Point out each Plasmodium parasite.
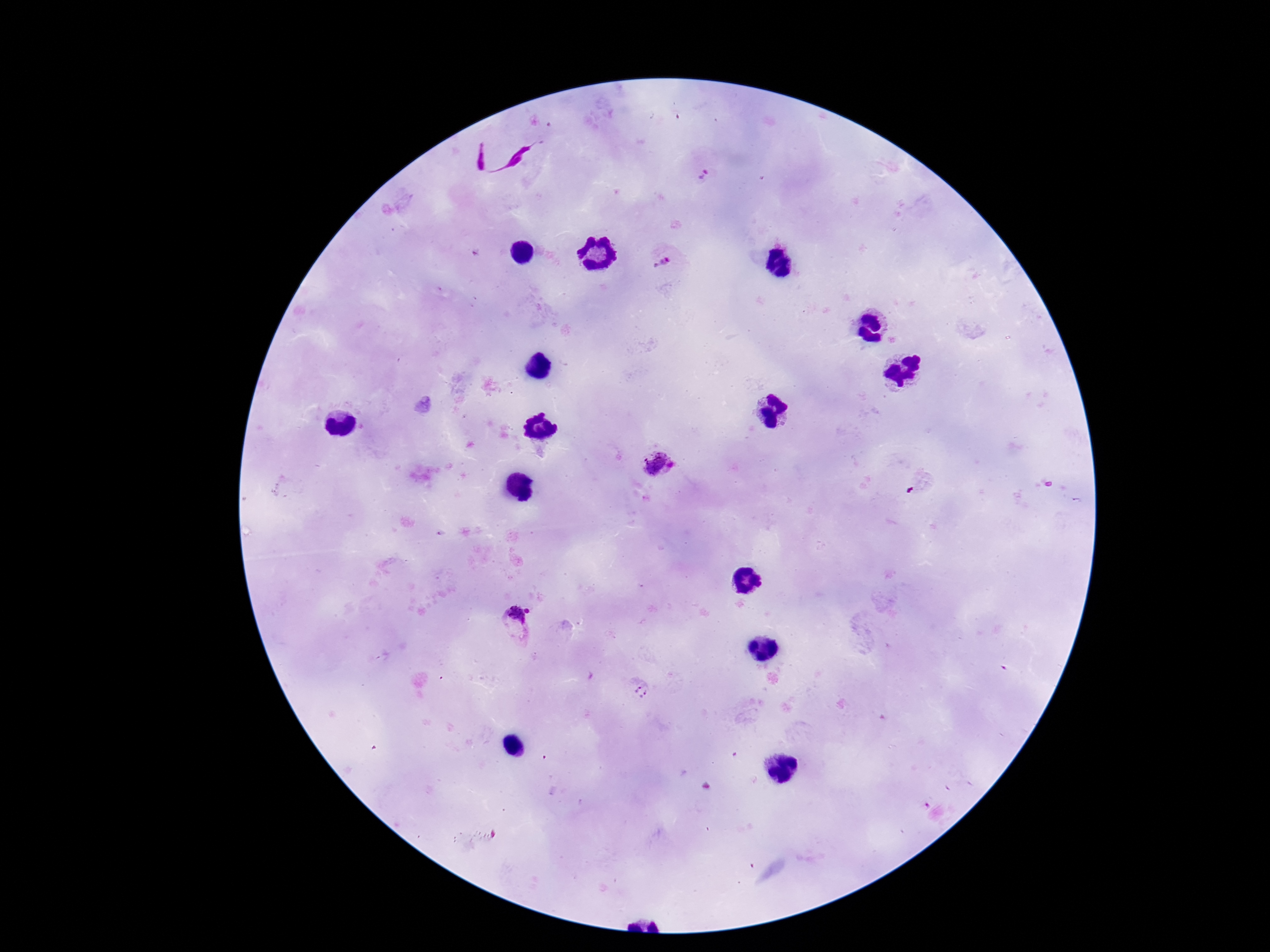

Approximate centers as [x, y] in pixels.
Plasmodium parasites: [702, 176], [662, 262], [658, 466], [515, 626], [641, 690].

Image is 1270×952 pixels. Single field of view. Patient malaria status: infected. 100x magnification. Giemsa-stained preparation. Smartphone photograph taken through the microscope eyepiece. Thick blood smear.